Classify this cell by malaria status.
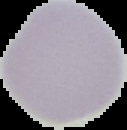
It is uninfected.

Summary:
  - Image size: 127×130 pixels
  - Image type: cell region segmented out of the field of view; surrounding area masked to black
  - Preparation: thin blood film